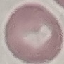

malaria status = uninfected
capture = smartphone camera at the microscope eyepiece
preparation = thin blood film
image type = automatically extracted cell patch, resized to 64 × 64 pixels
stain = Giemsa